Assess this cell for malaria.
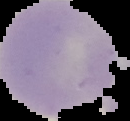

Uninfected.

Summary:
  - Image size: 130×121 pixels
  - Preparation: thin blood smear
  - Image type: cell region segmented out of the field of view; surrounding area masked to black